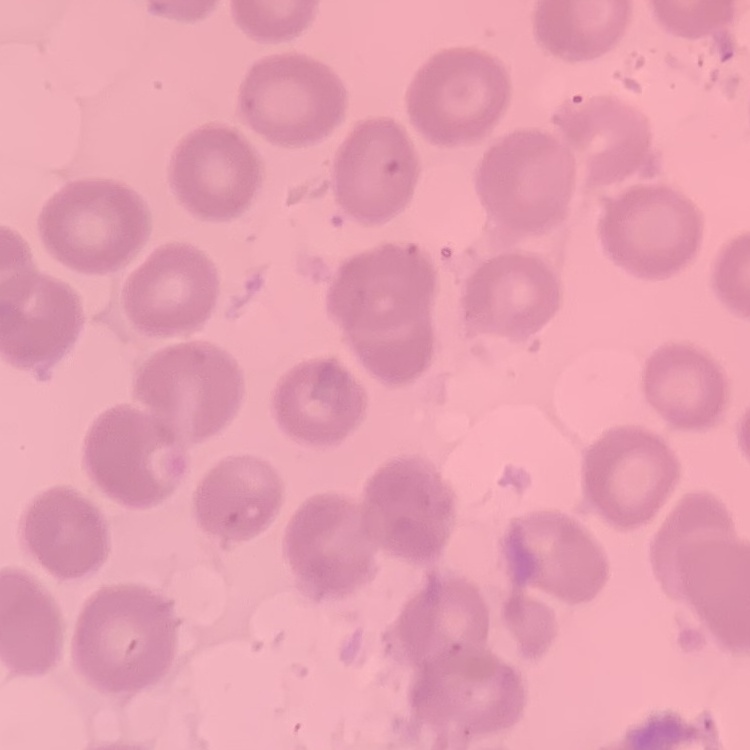

Summary:
  - Erythrocyte morphology: no rouleaux formation
  - Image type: one tile cut from a larger photomicrograph
  - Stain: Field's or Giemsa
  - Preparation: thin blood film